Assess the morphology of the erythrocytes.
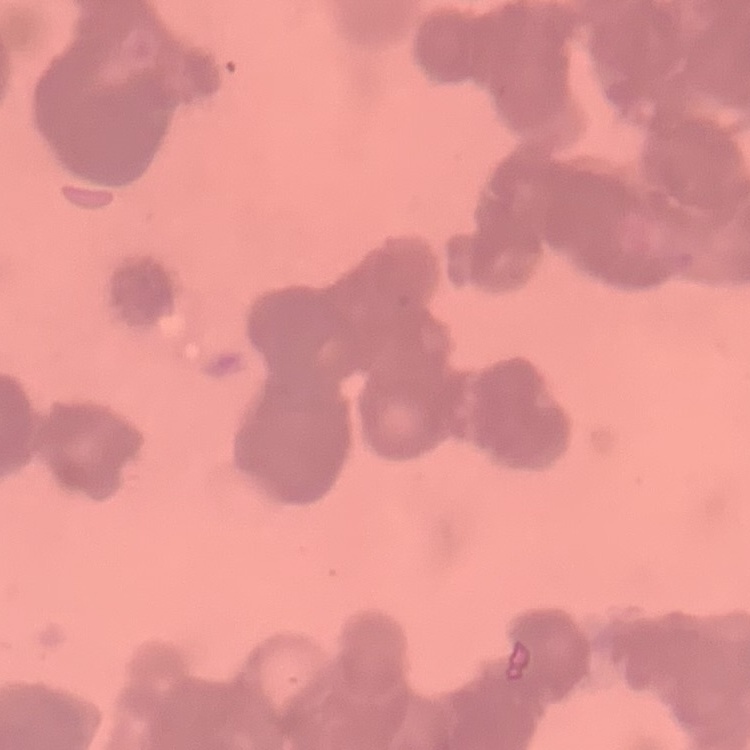
They show rouleaux formation.

stain: Field's or Giemsa
image_type: square crop of a larger photomicrograph
preparation: thin blood smear